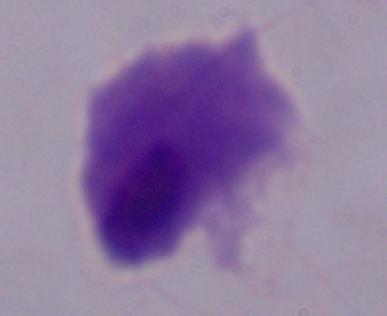

identification = trichomonad
magnification = 1000x
modality = micrograph